Name the blood parasite species.
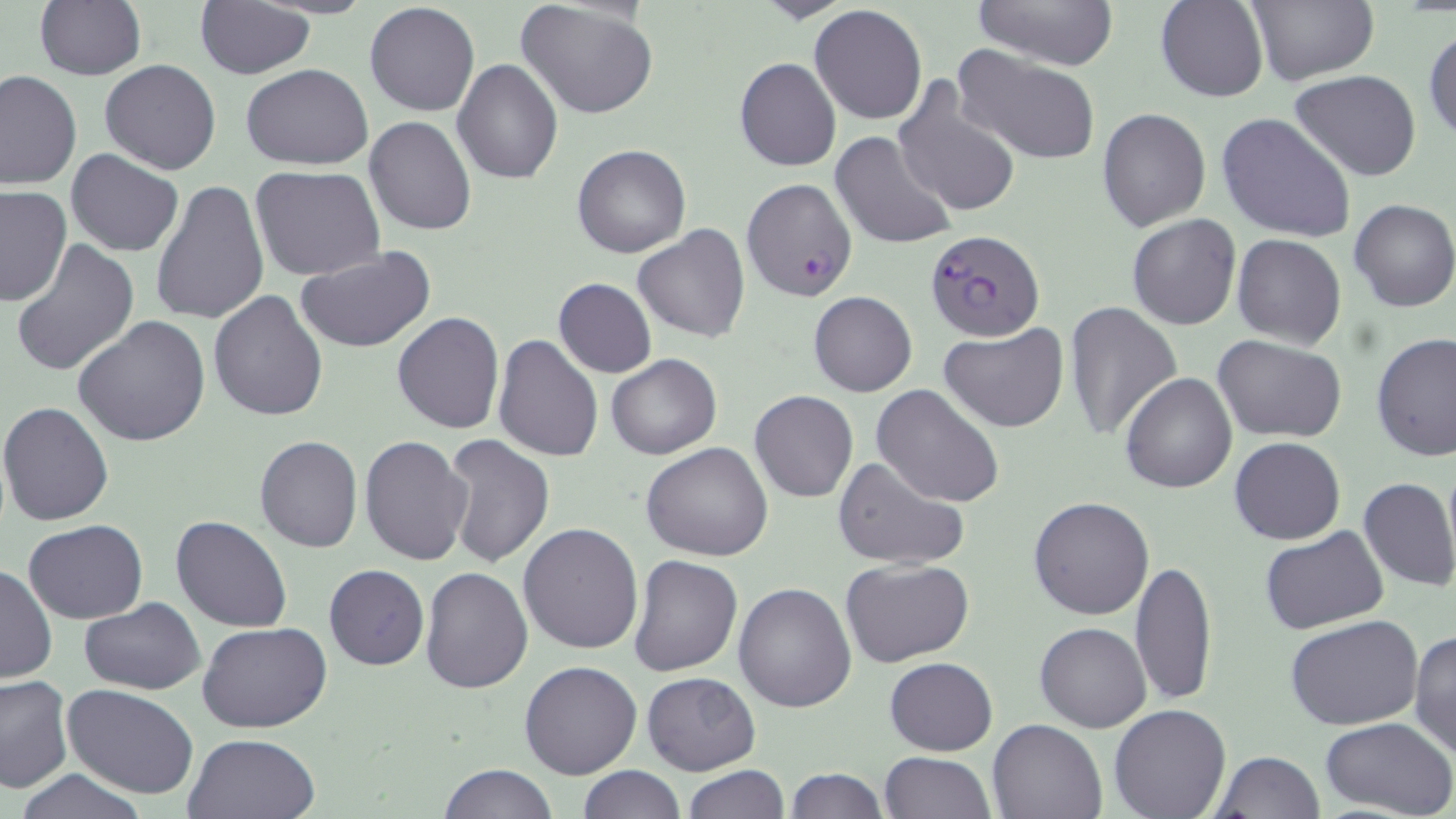

Plasmodium falciparum.

Approximate bounding boxes as named x1/y1/x2/y2 corners in pixels. Uninfected red blood cell locations: (x1=975, y1=0, x2=1118, y2=70), (x1=1156, y1=0, x2=1268, y2=103), (x1=514, y1=1, x2=658, y2=121), (x1=1246, y1=1, x2=1378, y2=86), (x1=33, y1=2, x2=147, y2=81), (x1=194, y1=2, x2=316, y2=79), (x1=364, y1=3, x2=479, y2=117), (x1=809, y1=5, x2=928, y2=126), (x1=1425, y1=25, x2=1456, y2=144), (x1=951, y1=45, x2=1102, y2=165), (x1=452, y1=58, x2=562, y2=183), (x1=734, y1=58, x2=841, y2=172), (x1=99, y1=60, x2=221, y2=175), (x1=240, y1=64, x2=373, y2=170), (x1=1, y1=70, x2=80, y2=190), (x1=1290, y1=70, x2=1421, y2=181), (x1=891, y1=78, x2=1022, y2=219), (x1=1097, y1=107, x2=1211, y2=231), (x1=1217, y1=112, x2=1355, y2=244), (x1=364, y1=115, x2=477, y2=237), (x1=829, y1=131, x2=957, y2=250), (x1=572, y1=143, x2=691, y2=257), (x1=65, y1=149, x2=184, y2=257), (x1=251, y1=165, x2=386, y2=280), (x1=152, y1=180, x2=269, y2=326), (x1=0, y1=186, x2=72, y2=306), (x1=1349, y1=199, x2=1456, y2=313), (x1=1126, y1=214, x2=1243, y2=330), (x1=634, y1=225, x2=750, y2=343), (x1=1232, y1=235, x2=1346, y2=351), (x1=10, y1=237, x2=140, y2=377), (x1=295, y1=247, x2=436, y2=354), (x1=552, y1=278, x2=657, y2=378), (x1=807, y1=290, x2=916, y2=396), (x1=207, y1=291, x2=329, y2=421), (x1=1062, y1=299, x2=1185, y2=441), (x1=391, y1=312, x2=505, y2=434), (x1=72, y1=315, x2=211, y2=448), (x1=940, y1=323, x2=1069, y2=432), (x1=495, y1=333, x2=604, y2=463), (x1=1371, y1=333, x2=1456, y2=462), (x1=1214, y1=335, x2=1347, y2=441), (x1=605, y1=354, x2=721, y2=458), (x1=1119, y1=372, x2=1237, y2=493), (x1=871, y1=383, x2=1006, y2=508), (x1=749, y1=389, x2=858, y2=502), (x1=0, y1=401, x2=115, y2=527), (x1=441, y1=435, x2=554, y2=569), (x1=254, y1=436, x2=362, y2=553), (x1=359, y1=436, x2=474, y2=566), (x1=1230, y1=436, x2=1345, y2=545), (x1=641, y1=441, x2=774, y2=561), (x1=831, y1=455, x2=970, y2=571), (x1=1357, y1=476, x2=1456, y2=592), (x1=1028, y1=496, x2=1155, y2=620), (x1=170, y1=515, x2=293, y2=633), (x1=23, y1=520, x2=148, y2=622), (x1=517, y1=522, x2=645, y2=654), (x1=1261, y1=527, x2=1387, y2=635), (x1=630, y1=555, x2=744, y2=676), (x1=840, y1=557, x2=976, y2=669), (x1=1131, y1=558, x2=1218, y2=706), (x1=1, y1=562, x2=57, y2=683), (x1=324, y1=563, x2=429, y2=670), (x1=420, y1=567, x2=532, y2=694), (x1=733, y1=582, x2=856, y2=713), (x1=79, y1=598, x2=206, y2=694), (x1=1286, y1=615, x2=1425, y2=730), (x1=198, y1=622, x2=332, y2=732), (x1=1034, y1=622, x2=1151, y2=733), (x1=1409, y1=628, x2=1456, y2=759), (x1=885, y1=657, x2=997, y2=755), (x1=519, y1=660, x2=642, y2=780), (x1=642, y1=672, x2=761, y2=773), (x1=0, y1=674, x2=72, y2=793), (x1=61, y1=684, x2=199, y2=799), (x1=1108, y1=704, x2=1232, y2=819), (x1=1320, y1=716, x2=1456, y2=818), (x1=987, y1=717, x2=1109, y2=818), (x1=182, y1=731, x2=320, y2=818), (x1=879, y1=750, x2=994, y2=818), (x1=1211, y1=751, x2=1325, y2=819), (x1=439, y1=763, x2=556, y2=819), (x1=682, y1=764, x2=790, y2=818), (x1=577, y1=765, x2=686, y2=819), (x1=785, y1=767, x2=887, y2=819), (x1=13, y1=769, x2=153, y2=819). Plasmodium falciparum-infected red blood cell locations: (x1=741, y1=177, x2=856, y2=302), (x1=925, y1=229, x2=1045, y2=341). Light microscopy. Single field of view. Image is 1456×819 pixels. Thin blood smear. May-Grünwald-Giemsa-stained preparation. Captured at 1000x magnification.